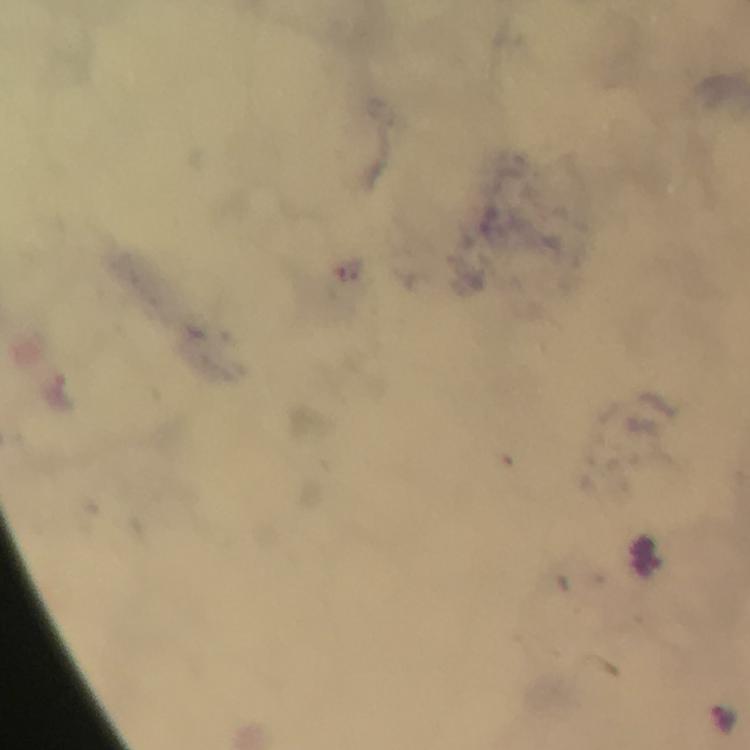

Approximate object centers, in pixels from the top-left corner. Malaria parasite locations: (x=721, y=720). 100x magnification. Immersion oil was used. From a diagnostic examination for malaria. Thick smear. Image is 750×750 pixels. Photographed with a smartphone mounted on the microscope. A crop from one field of view. Giemsa-stained preparation.